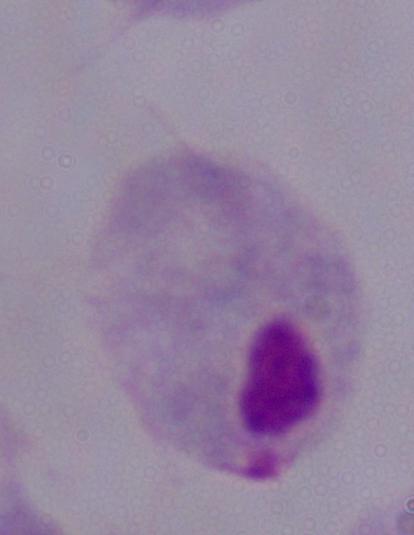
magnification = 1000x
identification = trichomonad
modality = micrograph